Assess this cell for malaria.
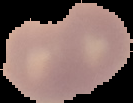

Uninfected.

preparation = thin blood smear
image size = 133×103 pixels
image type = segmented cell region with the area outside set to black